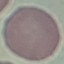

Summary:
  - Malaria status: uninfected
  - Image type: cell patch, automatically extracted from a larger field of view and resized to 64 × 64 pixels
  - Preparation: thin blood film
  - Capture: smartphone through the microscope eyepiece
  - Stain: Giemsa